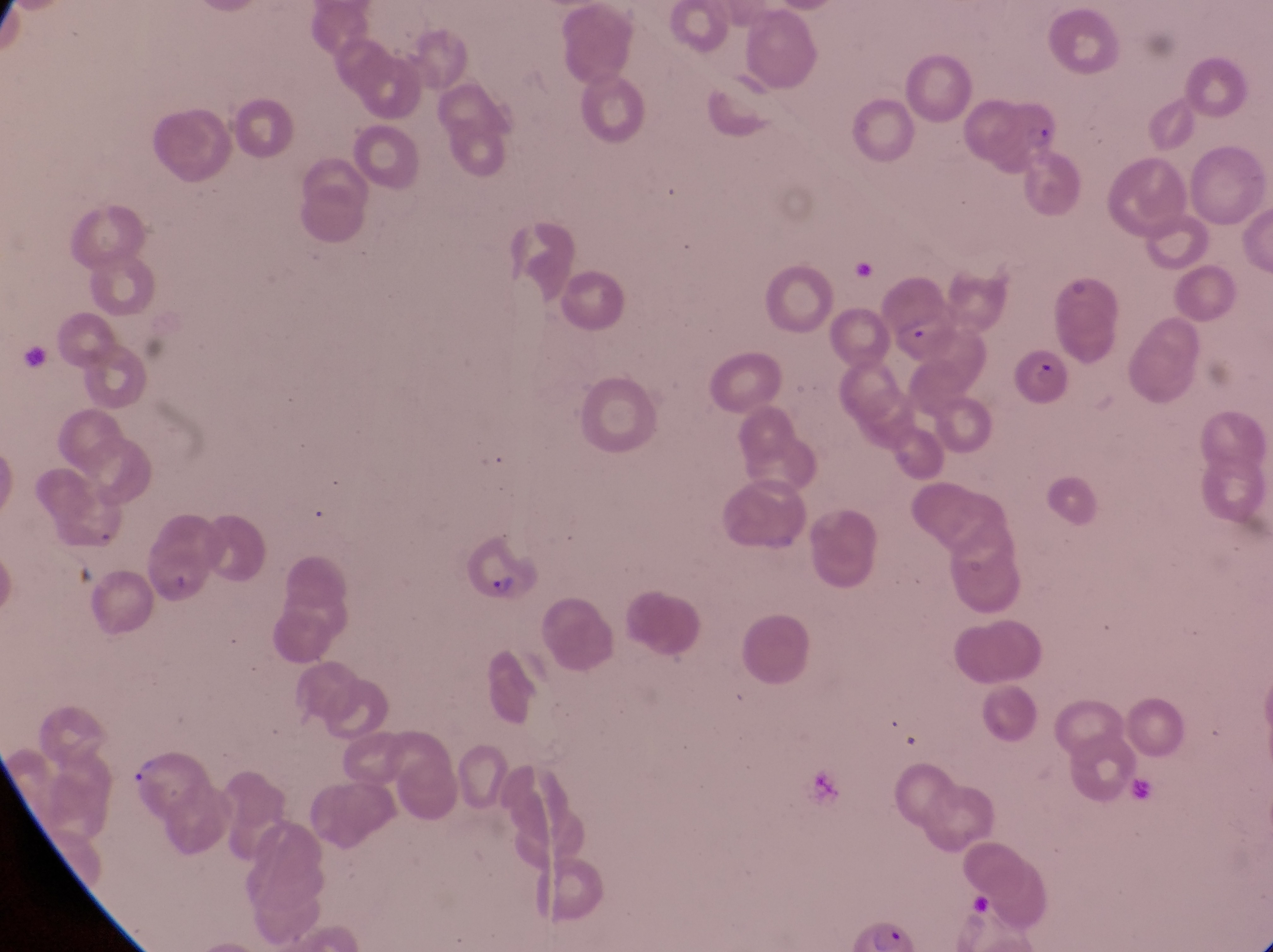
Approximate bounding boxes as [left, top, right, bottom] in pixels. Trophozoite locations: [125, 756, 165, 791]. Parasitised red blood cell locations: [1008, 93, 1063, 150], [1011, 348, 1078, 411], [457, 532, 535, 606]. At a magnification of 1000x. Collected in Uganda. Image is 1273×952 pixels. Thin blood smear. Photographed through the eyepiece of an Olympus CX-23 microscope with a smartphone camera. One field of view.